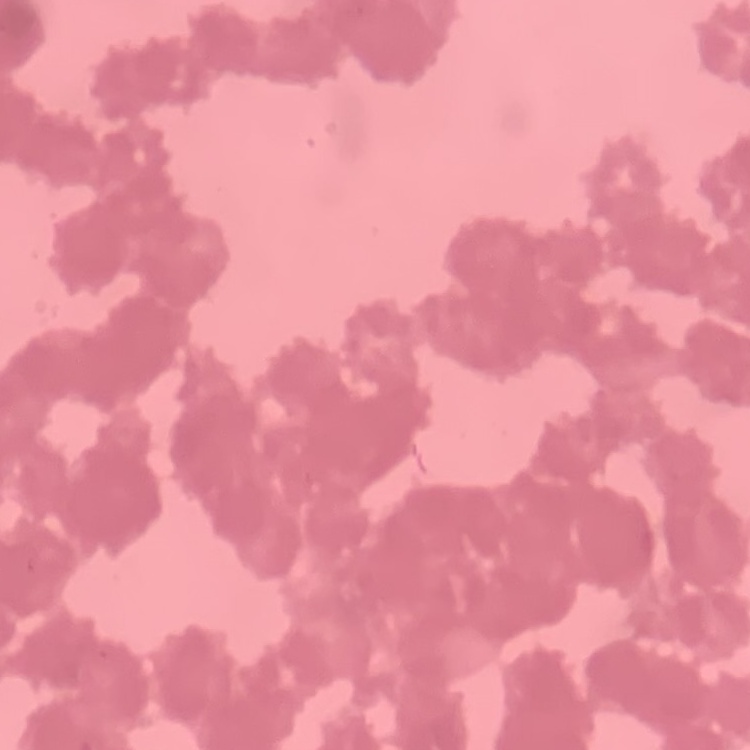

erythrocyte morphology = rouleaux formation
preparation = thin blood smear
stain = Field's or Giemsa
image type = one tile cut from a larger photomicrograph